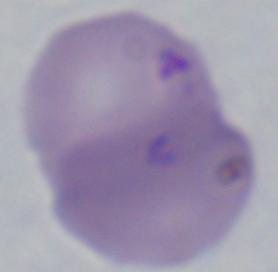

Summary:
  - Modality: photomicrograph
  - Magnification: 1000x
  - Identification: Babesia